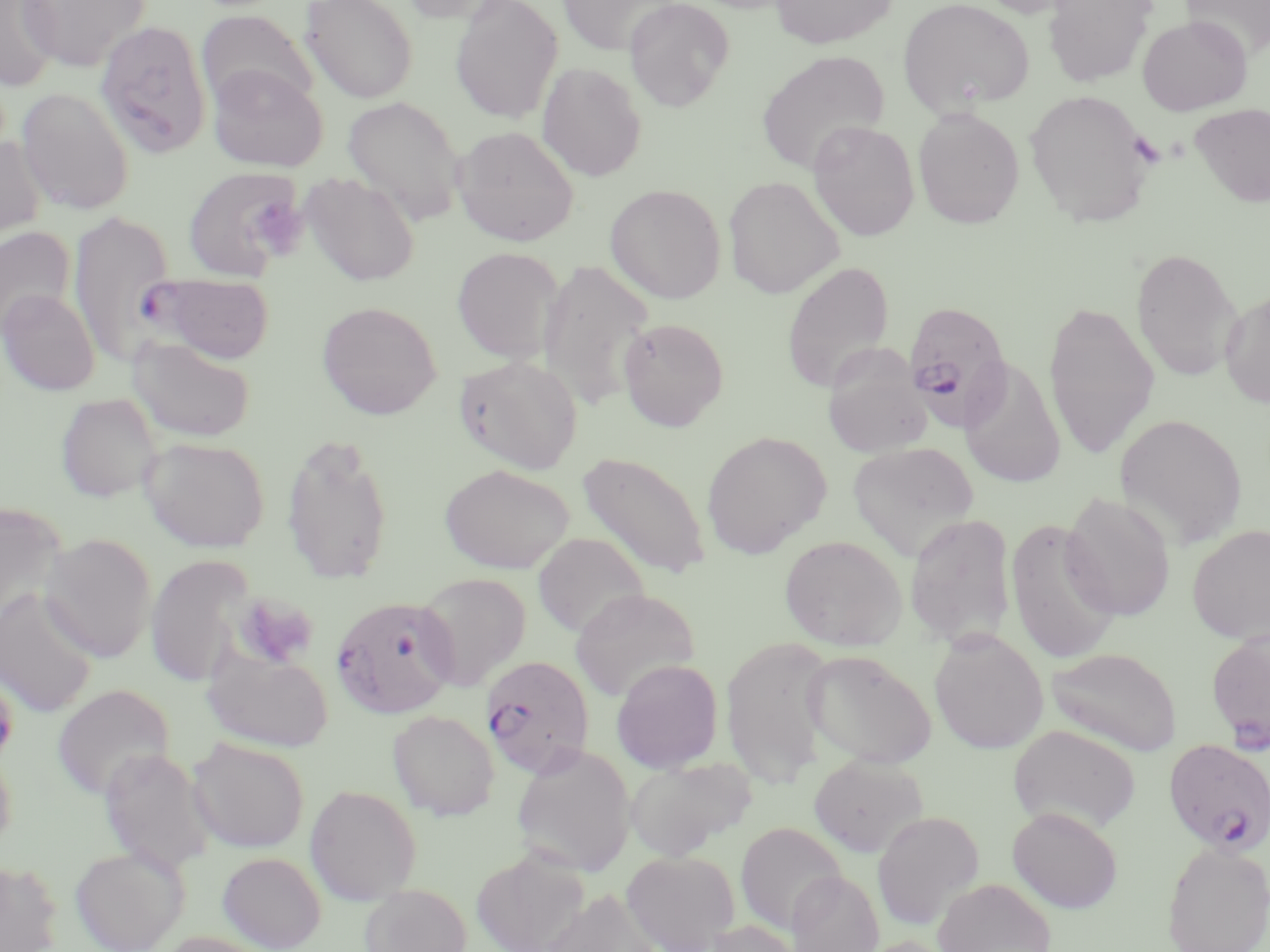

Summary:
  - Coordinate format: approximate bounding boxes as (x1,y1)-(x2,y2) corner pairs in pixels
  - Platelet locations: (1128,133)-(1166,169), (251,200)-(312,263), (232,592)-(319,670)
  - Uninfected red blood cell locations: (0,0)-(60,91), (18,0)-(150,71), (300,0)-(418,104), (396,0)-(515,25), (450,0)-(563,124), (556,0)-(683,56), (624,0)-(734,112), (770,0)-(897,48), (898,0)-(1035,116), (1043,0)-(1155,87), (1181,1)-(1270,58), (197,9)-(317,113), (1137,15)-(1252,115), (95,19)-(212,159), (756,50)-(889,174), (537,62)-(647,182), (208,64)-(328,172), (16,87)-(135,215), (1024,88)-(1156,227), (342,96)-(466,225), (1190,102)-(1270,208), (912,106)-(1025,229), (807,120)-(920,241), (452,125)-(579,246), (0,137)-(48,248), (181,165)-(305,281), (301,172)-(421,286), (723,175)-(844,298), (605,183)-(727,304), (66,210)-(175,367), (0,227)-(75,338), (451,246)-(565,363), (1130,247)-(1244,381), (536,259)-(655,411), (781,260)-(895,393), (1,288)-(100,396), (1219,289)-(1270,408), (1043,299)-(1159,459), (316,300)-(443,419), (618,317)-(729,431), (130,335)-(257,442), (821,346)-(932,458), (453,354)-(584,474), (959,356)-(1067,491), (56,392)-(164,502), (1115,412)-(1248,550), (700,430)-(831,559), (280,432)-(395,585), (139,436)-(270,552), (848,441)-(980,561), (577,450)-(712,580), (440,463)-(574,574), (1060,491)-(1177,621), (0,503)-(68,633), (904,512)-(1017,650), (1005,517)-(1122,666), (1187,524)-(1270,644), (532,532)-(649,639), (39,533)-(157,662), (779,535)-(906,650), (145,553)-(257,688), (414,572)-(531,691), (0,587)-(98,718), (570,587)-(700,702), (928,629)-(1048,755), (1206,629)-(1270,751), (721,636)-(835,786), (201,644)-(333,752), (1047,646)-(1182,755), (804,650)-(937,769), (611,659)-(723,774), (51,683)-(175,800), (388,710)-(499,820), (1008,724)-(1142,835), (187,736)-(310,853), (0,742)-(17,857), (511,745)-(636,878), (99,747)-(218,876), (808,755)-(928,858), (625,756)-(756,861), (304,784)-(422,905), (1007,807)-(1123,913), (872,811)-(984,929), (735,821)-(847,933), (1161,842)-(1270,952), (69,845)-(188,952), (472,848)-(590,952), (621,849)-(740,952), (217,851)-(327,951), (0,860)-(63,952), (786,869)-(884,952), (933,877)-(1056,952), (360,883)-(472,952), (542,887)-(662,952), (701,919)-(803,952), (853,936)-(958,952)
  - Plasmodium falciparum-infected red blood cell locations: (134,274)-(275,364), (902,300)-(1013,432), (330,594)-(457,720), (479,655)-(594,778), (1163,738)-(1270,854)
  - Slide-level diagnosis: Plasmodium falciparum
  - Preparation: thin blood film
  - Image size: 1270×952 pixels
  - Modality: optical microscopy
  - Field of view: single
  - Stain: May-Grünwald-Giemsa
  - Magnification: 1000x